Outline every Plasmodium parasite.
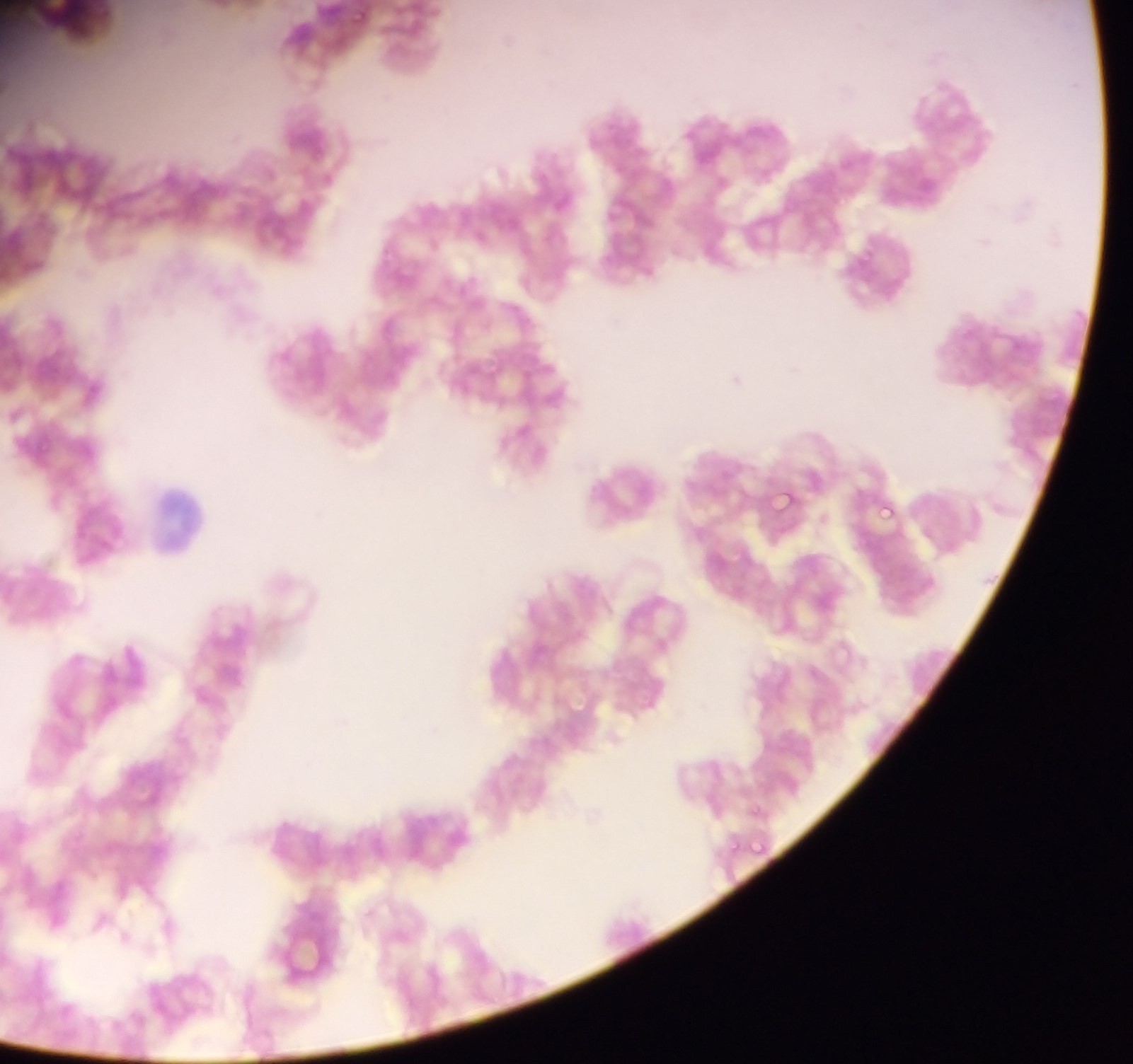
Approximate bounding boxes as left top right bottom in pixels.
Plasmodium parasites: 769 484 804 515; 877 501 897 523.

Leukocyte locations: 275 103 342 171; 153 489 210 545. Image is 1133×1064 pixels. Collected in Ghana. Thin blood smear. Mobile-phone photograph taken through the microscope. Single field of view.